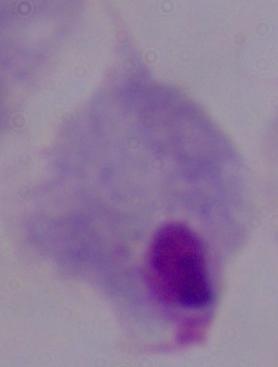
magnification: 1000x
identification: trichomonad
modality: photomicrograph